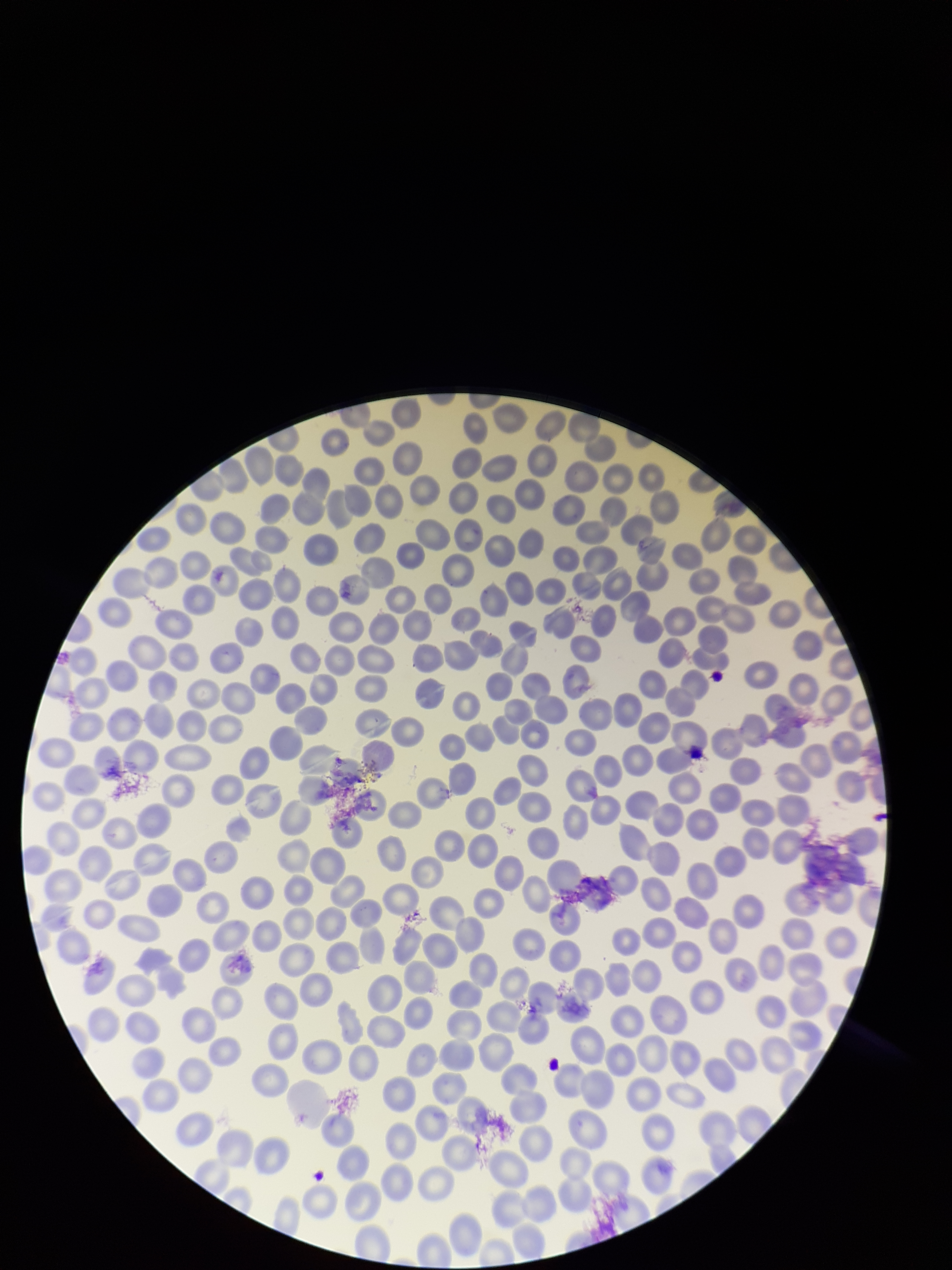
Preparation: thin smear. Smartphone photograph taken through the eyepiece of a microscope. Image is 952×1270 pixels. Red blood cell count: 303. Parasitized red blood cell count: 0. One field from this slide. Parasitized red blood cells: none seen. Patient malaria status: negative. Giemsa stain.